Assess for malaria.
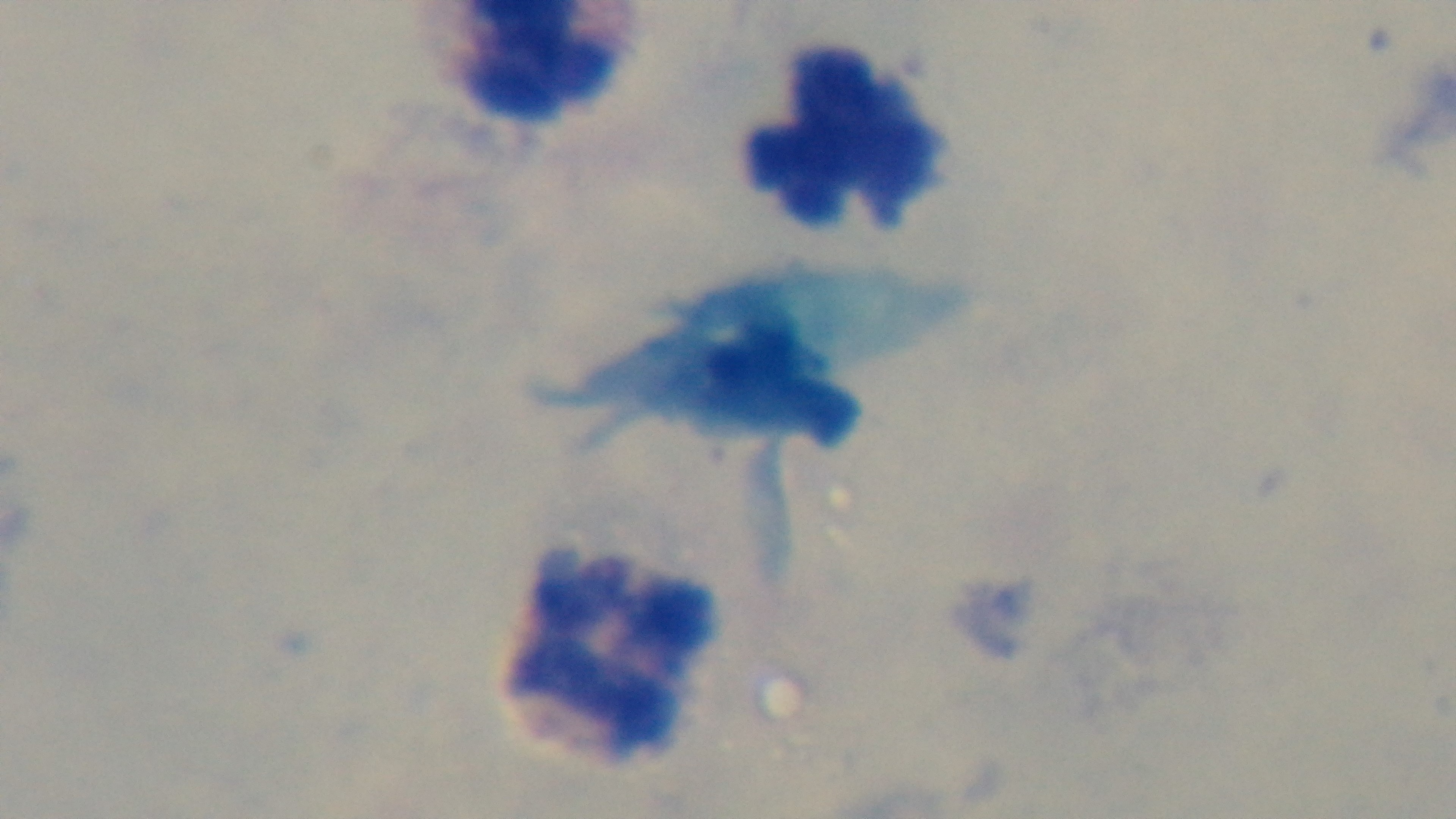

It is uninfected.

Summary:
  - Modality: light microscopy
  - Stain: Giemsa
  - Preparation: thick smear
  - Capture: mounted 4K digital camera
  - Objective: 100x oil immersion
  - Field of view: single